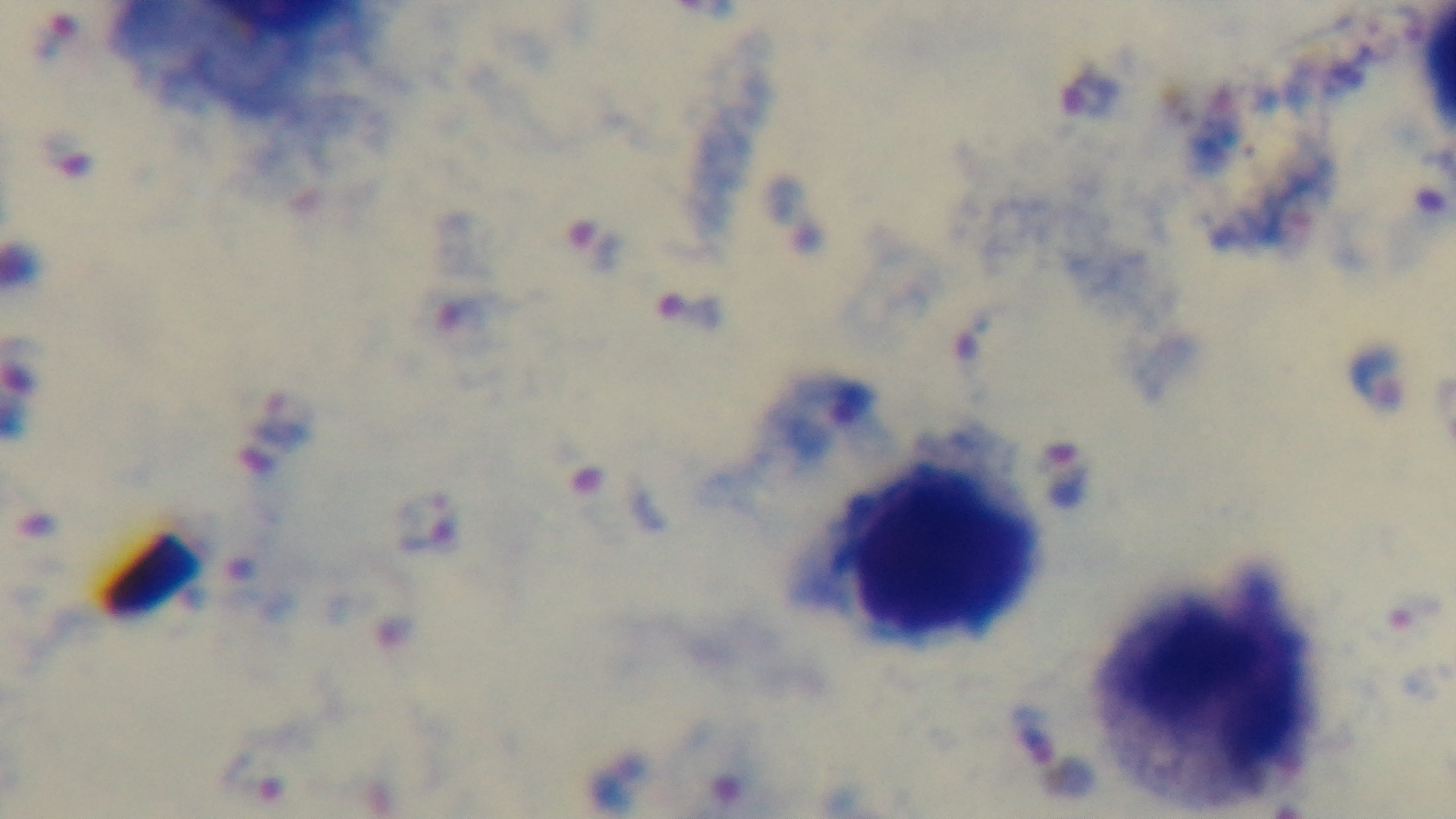

Summary:
  - Preparation: thick blood film
  - Capture: mounted 4K digital camera
  - Objective: 100x oil immersion
  - Field of view: single
  - Malaria status: infected
  - Modality: light microscopy
  - Stain: Giemsa